Describe the morphology of the red blood cells.
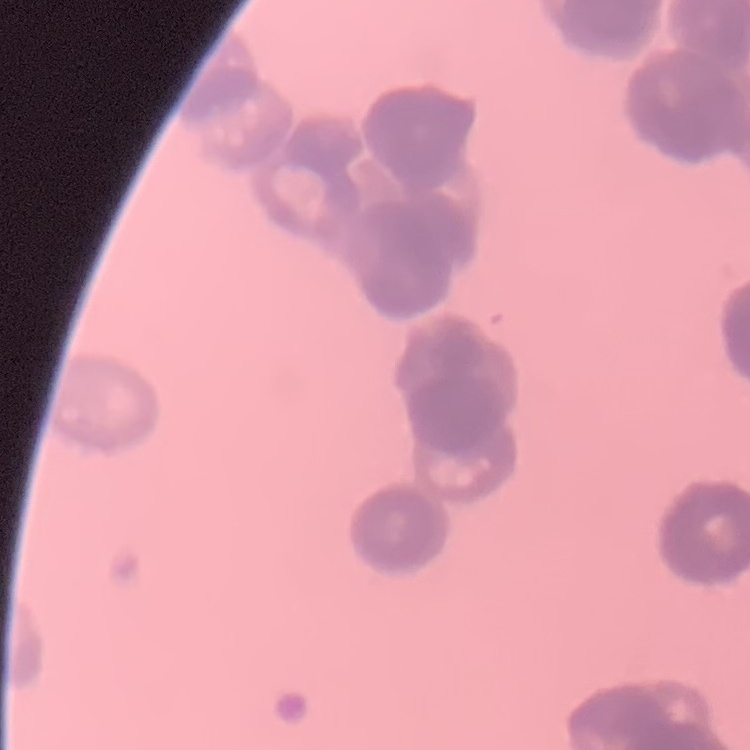

They show rouleaux formation.

Thin blood smear. Stained with either Field's or Giemsa. Square crop of a larger photomicrograph.